Assess this cell for malaria.
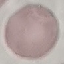

Uninfected.

Summary:
  - Stain: Giemsa
  - Image type: automatically extracted cell patch, resized to 64 × 64 pixels
  - Preparation: thin blood smear
  - Capture: smartphone through the microscope eyepiece